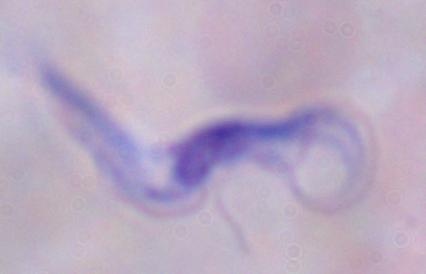
Summary:
  - Magnification: 1000x
  - Identification: trypanosome
  - Modality: photomicrograph